Name the blood parasite species.
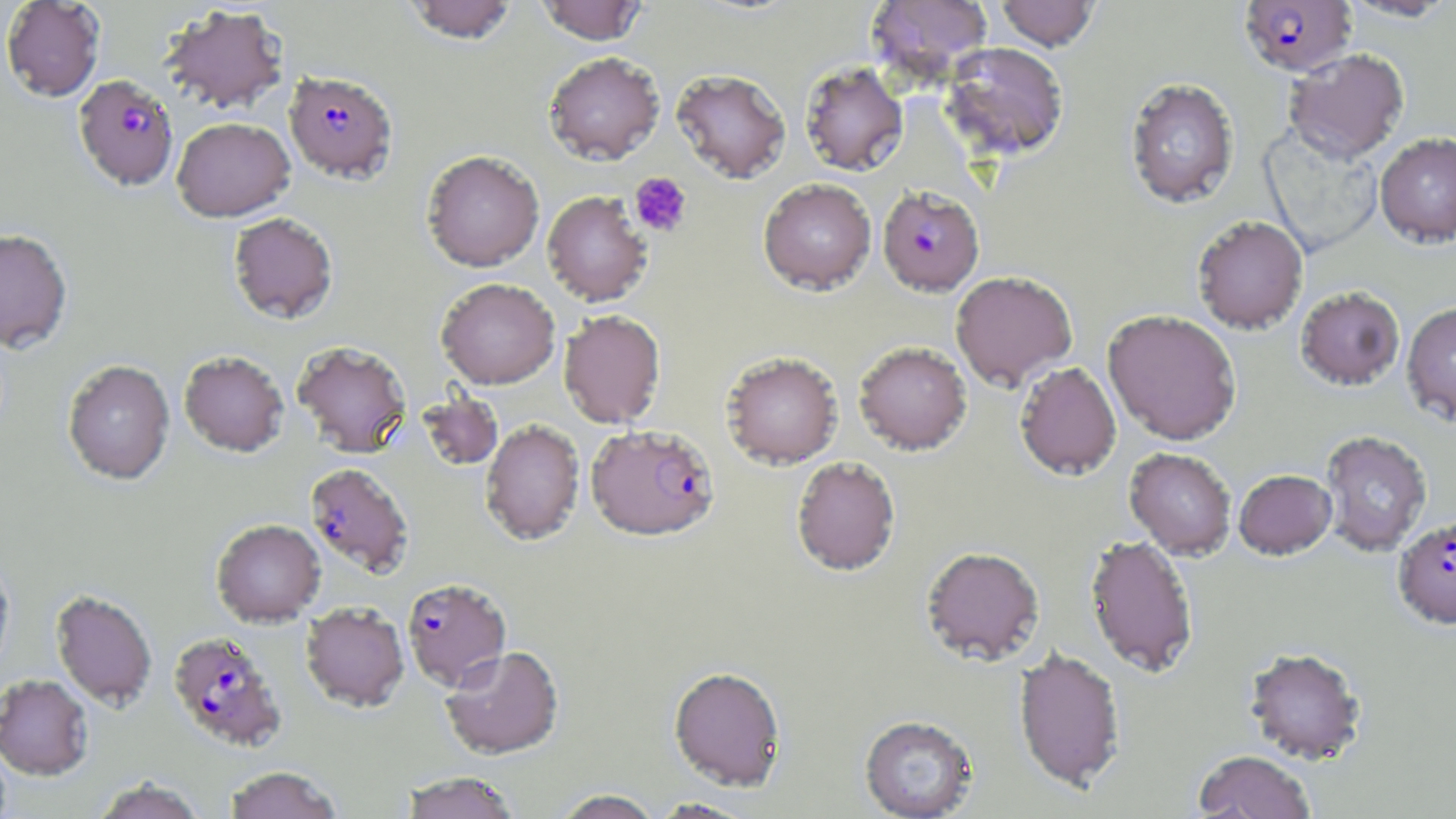

Plasmodium falciparum.

{
  "platelet_locations": "approximate bounding boxes as (x1,y1)-(x2,y2) corner pairs in pixels: (629,172)-(693,237)",
  "magnification": "1000x",
  "uninfected_red_blood_cell_locations": "approximate bounding boxes as (x1,y1)-(x2,y2) corner pairs in pixels: (1,0)-(106,102), (402,0)-(519,44), (536,0)-(648,45), (866,0)-(994,88), (995,0)-(1100,51), (1339,0)-(1455,22), (159,4)-(290,114), (940,42)-(1070,161), (1283,48)-(1410,164), (544,51)-(665,165), (799,61)-(909,176), (671,68)-(791,184), (1125,77)-(1240,209), (172,117)-(295,222), (1259,127)-(1383,258), (1374,133)-(1456,249), (421,150)-(544,272), (758,178)-(877,295), (542,191)-(653,307), (228,213)-(339,326), (1192,216)-(1308,335), (0,228)-(73,352), (950,271)-(1078,391), (436,279)-(560,390), (1296,287)-(1405,391), (1401,303)-(1456,428), (558,311)-(665,429), (1103,311)-(1241,446), (292,341)-(412,458), (853,341)-(973,455), (178,351)-(289,458), (721,352)-(843,469), (62,360)-(175,486), (1014,362)-(1122,481), (418,393)-(504,471), (480,420)-(585,546), (1320,431)-(1432,557), (1124,448)-(1237,560), (791,457)-(901,576), (1234,470)-(1337,561), (211,520)-(325,629), (1084,536)-(1199,679), (920,548)-(1045,666), (0,557)-(15,682), (50,589)-(157,711), (301,604)-(409,714), (440,646)-(564,762), (1244,648)-(1368,766), (1013,649)-(1127,794), (668,667)-(786,793), (0,675)-(94,781), (859,716)-(978,819), (1193,751)-(1316,819), (224,767)-(342,819), (401,772)-(520,819), (93,777)-(206,819), (552,790)-(663,819), (649,797)-(757,818)",
  "modality": "light microscopy",
  "image_size": "1456×819 pixels",
  "preparation": "thin blood smear",
  "stain": "May-Grünwald-Giemsa",
  "field_of_view": "single",
  "plasmodium_falciparum_infected_red_blood_cell_locations": "approximate bounding boxes as (x1,y1)-(x2,y2) corner pairs in pixels: (1238,0)-(1358,77), (284,70)-(398,183), (73,75)-(179,191), (877,186)-(984,296), (587,418)-(721,537), (304,463)-(414,578), (1393,515)-(1456,631), (402,579)-(512,692), (168,631)-(288,753)"
}